Point out each Plasmodium parasite.
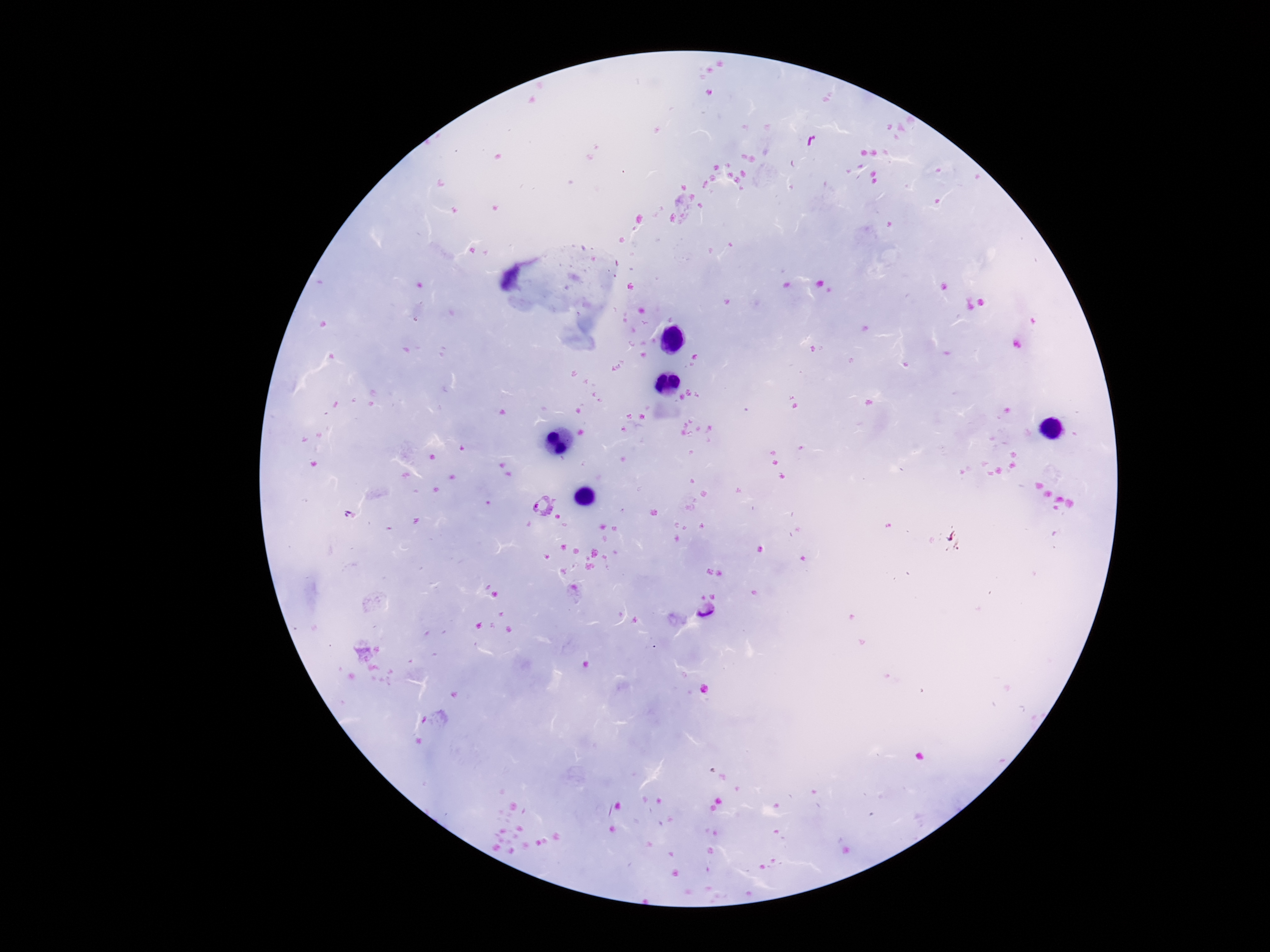

Approximate object centers, in pixels from the top-left corner.
Plasmodium parasites: (x=542, y=506), (x=708, y=610).

Thick blood smear. Single field of view. Smartphone photograph taken through the microscope eyepiece. Patient malaria status: positive. Image is 1270×952 pixels. Giemsa stain. 100x magnification.